State the blood parasite species.
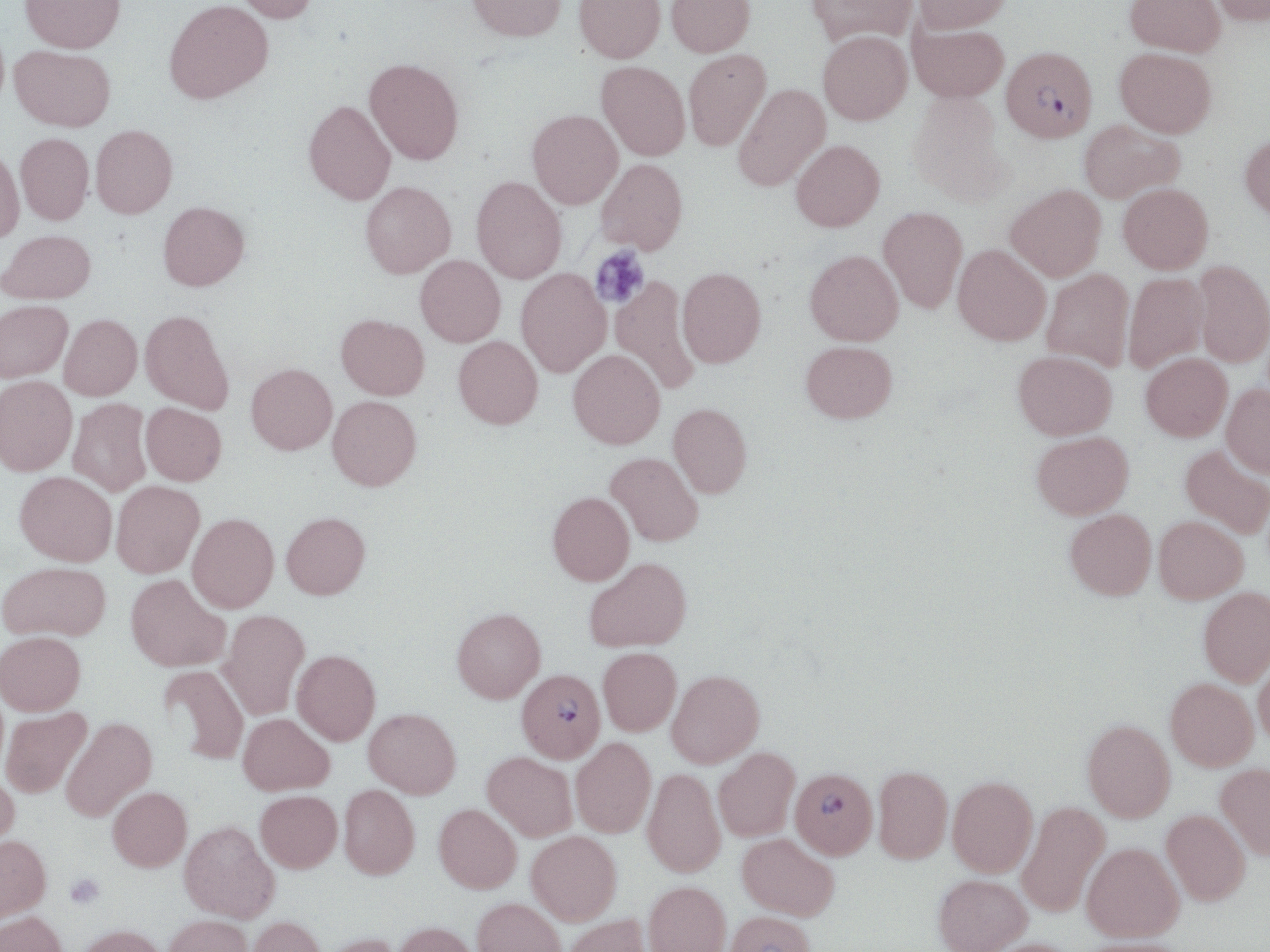
Plasmodium falciparum.

Summary:
  - Coordinate format: approximate bounding boxes as named x1/y1/x2/y2 corners in pixels
  - Plasmodium falciparum-infected red blood cell locations: (x1=1002, y1=46, x2=1097, y2=143), (x1=517, y1=669, x2=605, y2=762), (x1=790, y1=768, x2=878, y2=858)
  - Platelet locations: (x1=590, y1=245, x2=650, y2=309), (x1=65, y1=873, x2=105, y2=910)
  - Uninfected red blood cell locations: (x1=21, y1=0, x2=125, y2=52), (x1=232, y1=0, x2=320, y2=23), (x1=466, y1=0, x2=567, y2=41), (x1=574, y1=0, x2=665, y2=63), (x1=666, y1=0, x2=755, y2=56), (x1=806, y1=0, x2=917, y2=47), (x1=913, y1=0, x2=1011, y2=33), (x1=1125, y1=0, x2=1226, y2=56), (x1=1207, y1=0, x2=1270, y2=27), (x1=164, y1=1, x2=272, y2=103), (x1=908, y1=23, x2=1008, y2=102), (x1=817, y1=30, x2=912, y2=125), (x1=9, y1=45, x2=115, y2=131), (x1=1114, y1=47, x2=1217, y2=138), (x1=683, y1=49, x2=771, y2=151), (x1=364, y1=58, x2=464, y2=164), (x1=596, y1=61, x2=690, y2=160), (x1=732, y1=83, x2=830, y2=192), (x1=907, y1=92, x2=1012, y2=205), (x1=304, y1=100, x2=396, y2=205), (x1=527, y1=109, x2=623, y2=209), (x1=1078, y1=120, x2=1185, y2=203), (x1=91, y1=125, x2=177, y2=218), (x1=15, y1=133, x2=94, y2=224), (x1=1240, y1=133, x2=1270, y2=223), (x1=791, y1=140, x2=884, y2=232), (x1=0, y1=149, x2=24, y2=243), (x1=595, y1=158, x2=687, y2=255), (x1=471, y1=176, x2=567, y2=283), (x1=360, y1=181, x2=456, y2=278), (x1=1118, y1=183, x2=1213, y2=274), (x1=1005, y1=184, x2=1106, y2=281), (x1=158, y1=201, x2=249, y2=290), (x1=878, y1=207, x2=967, y2=313), (x1=0, y1=230, x2=96, y2=303), (x1=953, y1=244, x2=1051, y2=345), (x1=804, y1=249, x2=903, y2=345), (x1=415, y1=255, x2=505, y2=346), (x1=1194, y1=261, x2=1270, y2=367), (x1=677, y1=267, x2=766, y2=367), (x1=516, y1=268, x2=611, y2=377), (x1=1041, y1=268, x2=1135, y2=371), (x1=1123, y1=272, x2=1208, y2=373), (x1=610, y1=276, x2=699, y2=394), (x1=0, y1=300, x2=73, y2=382), (x1=140, y1=309, x2=233, y2=414), (x1=59, y1=314, x2=142, y2=400), (x1=336, y1=314, x2=429, y2=399), (x1=453, y1=336, x2=543, y2=429), (x1=800, y1=340, x2=897, y2=423), (x1=568, y1=349, x2=665, y2=449), (x1=1013, y1=350, x2=1117, y2=440), (x1=1141, y1=353, x2=1232, y2=441), (x1=246, y1=363, x2=337, y2=454), (x1=0, y1=376, x2=77, y2=476), (x1=1222, y1=384, x2=1270, y2=478), (x1=327, y1=395, x2=422, y2=491), (x1=68, y1=398, x2=152, y2=497), (x1=141, y1=402, x2=226, y2=486), (x1=668, y1=403, x2=752, y2=498), (x1=1031, y1=431, x2=1133, y2=519), (x1=1180, y1=445, x2=1270, y2=538), (x1=606, y1=452, x2=703, y2=546), (x1=15, y1=471, x2=117, y2=566), (x1=111, y1=481, x2=204, y2=577), (x1=547, y1=492, x2=634, y2=585), (x1=1065, y1=509, x2=1156, y2=599), (x1=281, y1=511, x2=370, y2=599), (x1=188, y1=513, x2=279, y2=612), (x1=1154, y1=516, x2=1248, y2=603), (x1=584, y1=556, x2=692, y2=652), (x1=0, y1=561, x2=110, y2=641), (x1=126, y1=574, x2=230, y2=671), (x1=1198, y1=587, x2=1270, y2=685), (x1=452, y1=607, x2=546, y2=703), (x1=220, y1=609, x2=309, y2=719), (x1=0, y1=631, x2=86, y2=715), (x1=598, y1=647, x2=681, y2=735), (x1=292, y1=649, x2=380, y2=745), (x1=1253, y1=650, x2=1270, y2=745), (x1=158, y1=664, x2=249, y2=764), (x1=667, y1=670, x2=764, y2=767), (x1=1165, y1=678, x2=1258, y2=770), (x1=1, y1=707, x2=92, y2=798), (x1=364, y1=708, x2=461, y2=797), (x1=238, y1=713, x2=334, y2=795), (x1=61, y1=716, x2=156, y2=821), (x1=1082, y1=719, x2=1176, y2=822), (x1=571, y1=738, x2=655, y2=837), (x1=714, y1=748, x2=800, y2=841), (x1=482, y1=752, x2=577, y2=841), (x1=1215, y1=763, x2=1270, y2=860), (x1=873, y1=765, x2=953, y2=863), (x1=642, y1=768, x2=726, y2=877), (x1=0, y1=772, x2=20, y2=859), (x1=948, y1=777, x2=1038, y2=877), (x1=339, y1=784, x2=419, y2=879), (x1=107, y1=787, x2=192, y2=871), (x1=255, y1=790, x2=342, y2=872), (x1=1017, y1=801, x2=1110, y2=918), (x1=434, y1=803, x2=521, y2=892), (x1=1160, y1=809, x2=1250, y2=905), (x1=179, y1=820, x2=279, y2=922), (x1=527, y1=831, x2=622, y2=924), (x1=737, y1=833, x2=839, y2=920), (x1=0, y1=834, x2=51, y2=923), (x1=1082, y1=842, x2=1184, y2=943), (x1=934, y1=874, x2=1032, y2=952), (x1=644, y1=880, x2=731, y2=952), (x1=472, y1=897, x2=565, y2=952), (x1=0, y1=911, x2=68, y2=952), (x1=725, y1=911, x2=815, y2=952), (x1=563, y1=914, x2=655, y2=952), (x1=162, y1=915, x2=252, y2=952), (x1=247, y1=916, x2=326, y2=952), (x1=392, y1=921, x2=479, y2=952), (x1=75, y1=924, x2=167, y2=952), (x1=318, y1=932, x2=403, y2=952), (x1=982, y1=937, x2=1082, y2=952), (x1=1078, y1=937, x2=1194, y2=952)
  - Preparation: thin blood smear
  - Field of view: single
  - Stain: May-Grünwald-Giemsa
  - Image size: 1270×952 pixels
  - Modality: light microscopy
  - Magnification: 1000x